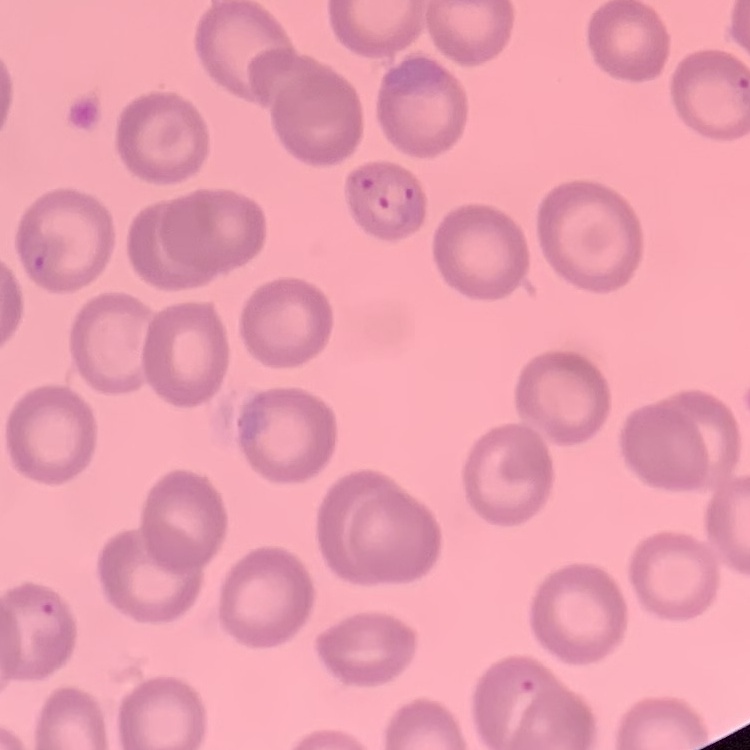

Summary:
  - Red blood cell morphology: no rouleaux formation
  - Image type: one tile cut from a larger photomicrograph
  - Preparation: thin peripheral smear
  - Stain: Field's or Giemsa